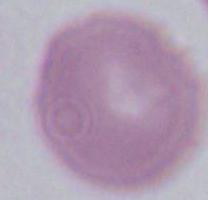
modality: photomicrograph
magnification: 1000x
identification: erythrocyte